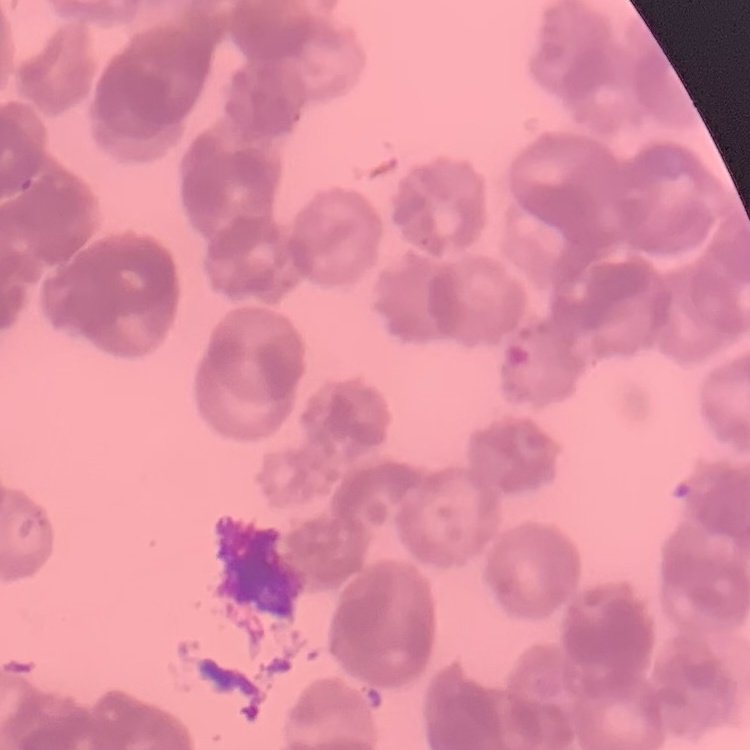

erythrocyte_morphology: rouleaux formation
image_type: square crop of a larger photomicrograph
stain: Field's or Giemsa
preparation: thin blood film